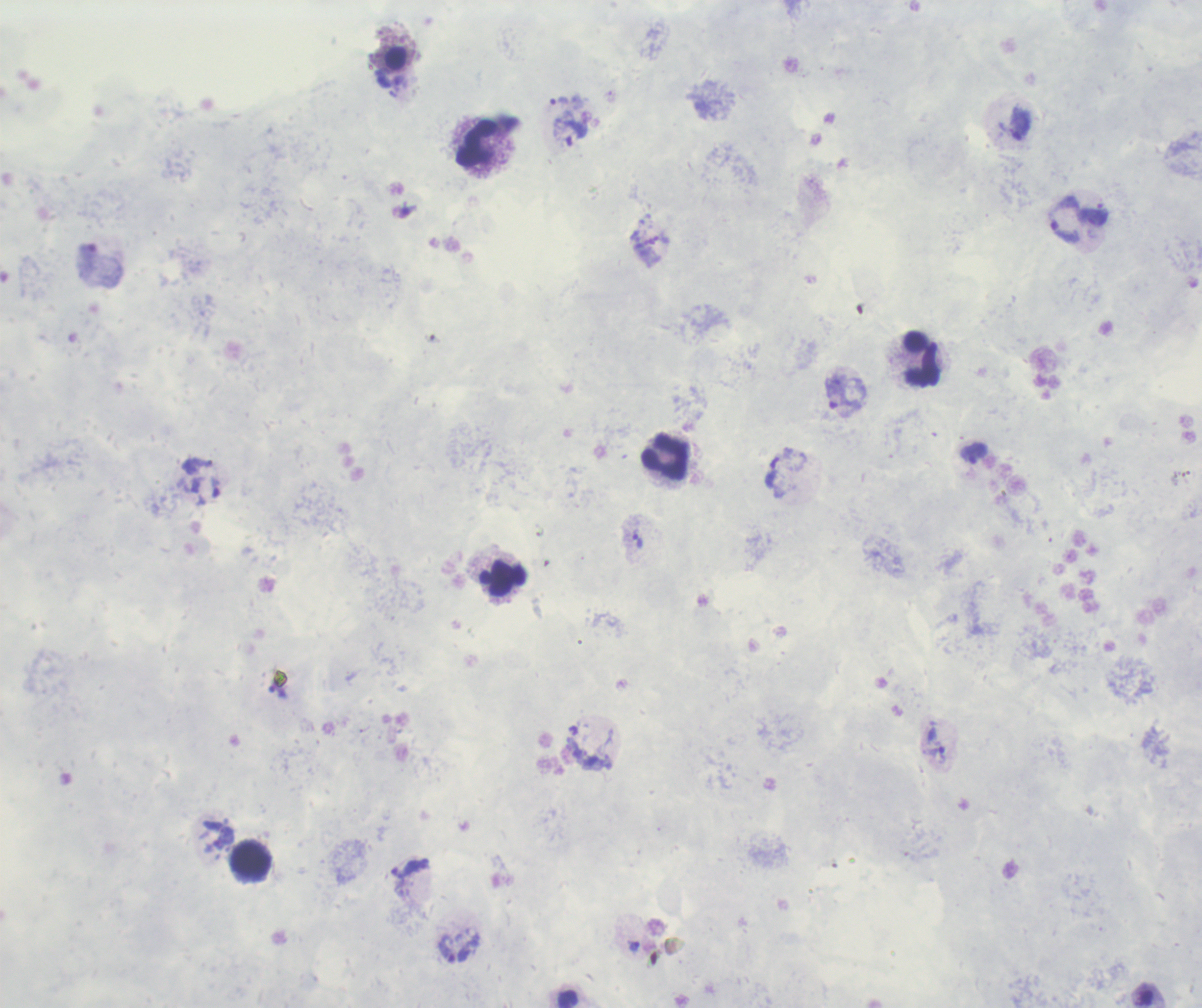

Approximate object centers, in pixels from the top-left corner.
Summary:
  - Trophozoite locations: (x=1020, y=123), (x=569, y=132), (x=1064, y=220), (x=836, y=392), (x=973, y=453), (x=637, y=540), (x=278, y=691), (x=934, y=756), (x=410, y=868), (x=633, y=946), (x=447, y=948)
  - Leukocyte locations: (x=476, y=144), (x=921, y=359), (x=664, y=457), (x=501, y=578), (x=251, y=859)
  - Image size: 1202×1008 pixels
  - Stain: Romanowsky
  - Result: positive for Plasmodium parasites
  - Magnification: 100x
  - Coloration quality: bad
  - Background quality: unsatisfactory
  - Context: previously used in a real diagnosis
  - Preparation: thick blood smear
  - Field of view: single